Classify this cell by malaria status.
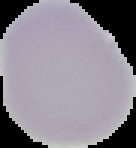
Uninfected.

Segmented cell region on a black background. Image is 136×148 pixels. From a thin blood smear.